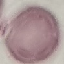
Summary:
  - Result: no malaria parasites detected
  - Capture: smartphone camera at the microscope eyepiece
  - Stain: Giemsa
  - Image type: cell patch, automatically extracted from a larger field of view and resized to 64 × 64 pixels
  - Preparation: thin smear